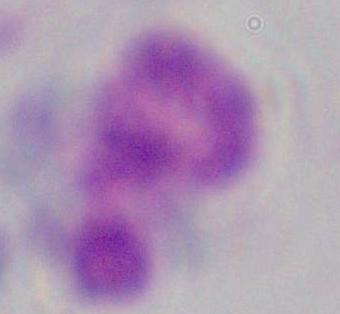

identification = white blood cell
magnification = 1000x
modality = micrograph